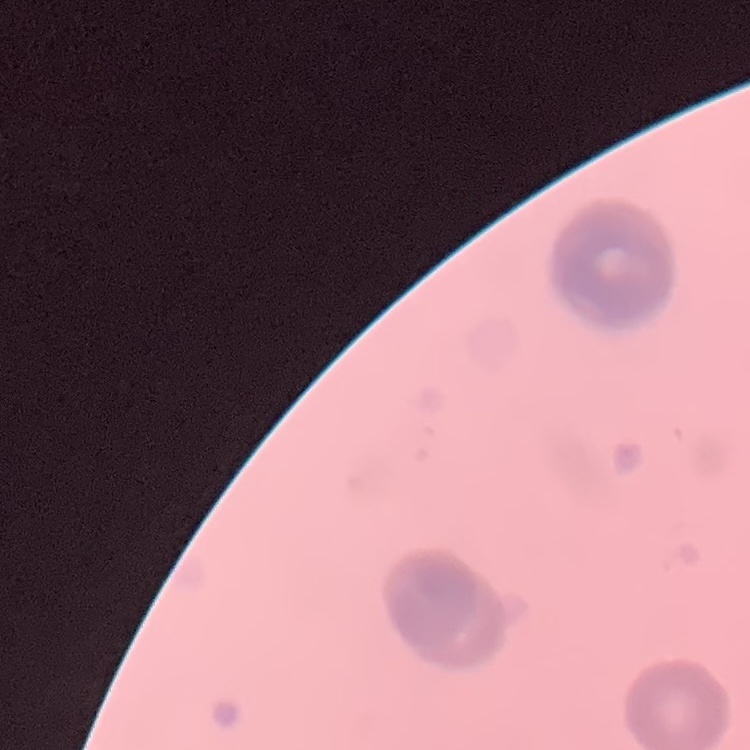

erythrocyte morphology = rouleaux formation
stain = Field's or Giemsa
image type = one tile cut from a larger photomicrograph
preparation = thin peripheral smear